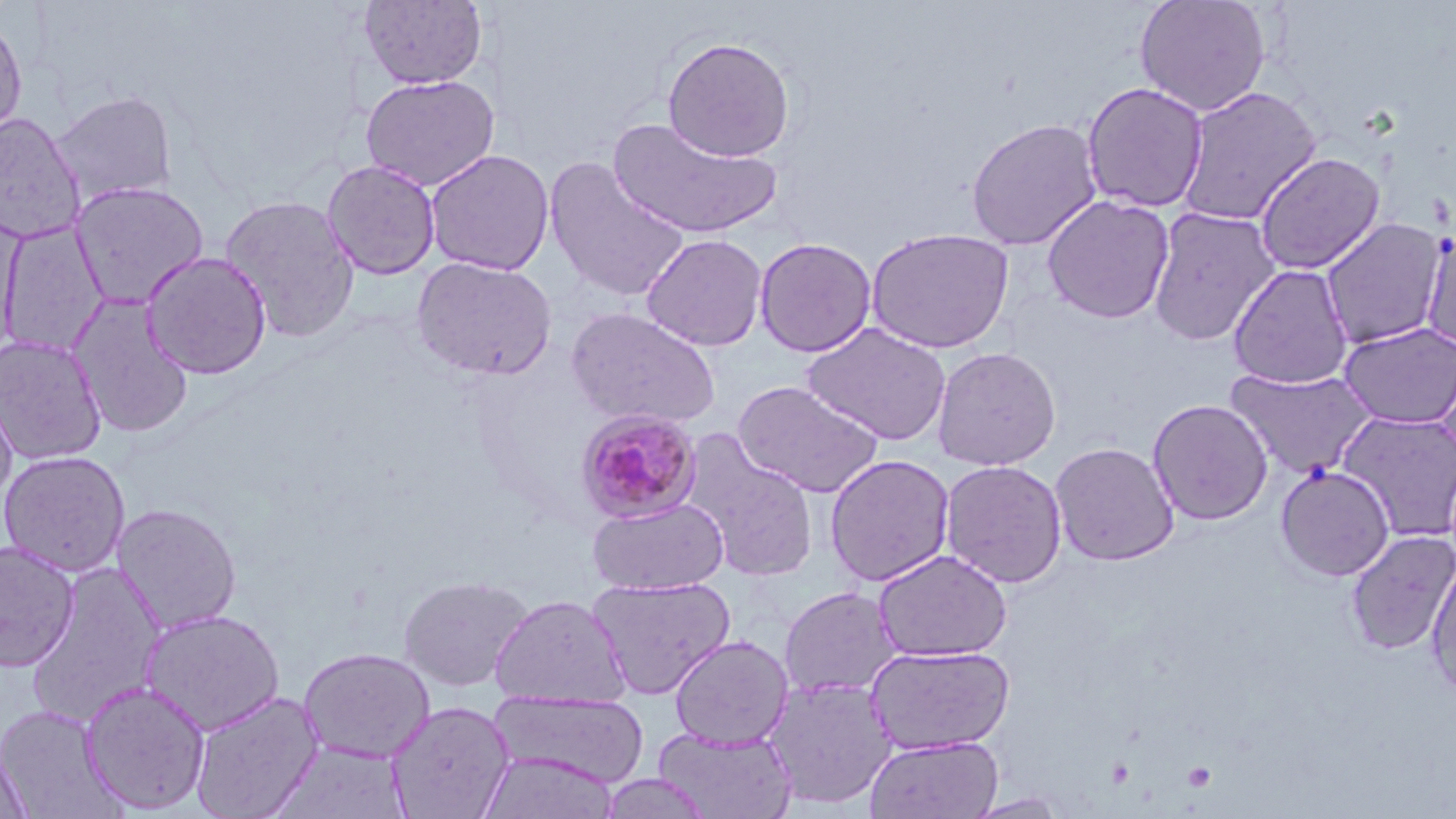
Approximate bounding boxes as (x1,y1)-(x2,y2) corner pairs in pixels. Uninfected red blood cell locations: (357,0)-(489,89), (1134,0)-(1272,117), (0,12)-(28,141), (662,37)-(796,162), (361,74)-(500,191), (1081,81)-(1209,213), (1176,85)-(1322,227), (50,90)-(178,207), (0,113)-(85,244), (607,116)-(783,240), (965,117)-(1103,250), (425,148)-(555,276), (1254,151)-(1385,275), (545,157)-(689,303), (321,160)-(441,280), (69,181)-(208,309), (219,194)-(360,344), (1041,194)-(1175,324), (1147,206)-(1281,347), (0,213)-(21,361), (1319,218)-(1449,349), (0,222)-(109,358), (1420,226)-(1456,355), (865,227)-(1014,354), (641,233)-(768,351), (754,237)-(877,357), (140,251)-(272,380), (411,256)-(557,381), (1228,263)-(1354,390), (67,294)-(195,440), (565,307)-(721,430), (802,322)-(952,446), (1338,322)-(1456,430), (0,334)-(108,465), (931,346)-(1061,471), (1432,354)-(1456,478), (1226,366)-(1378,480), (732,380)-(884,498), (0,390)-(17,507), (1147,399)-(1273,526), (1335,410)-(1456,541), (685,441)-(820,582), (1048,441)-(1180,566), (0,450)-(131,577), (824,454)-(955,587), (939,459)-(1068,589), (1275,465)-(1395,582), (588,498)-(728,595), (112,503)-(243,634), (1345,530)-(1456,655), (0,541)-(80,673), (873,549)-(1012,662), (1425,554)-(1456,700), (25,562)-(169,730), (398,575)-(532,691), (586,576)-(737,698), (779,585)-(902,700), (489,594)-(630,707), (139,608)-(285,736), (670,635)-(794,749), (866,644)-(1015,755), (298,647)-(435,763), (763,675)-(897,810), (80,680)-(211,814), (489,690)-(650,788), (190,691)-(323,819), (385,700)-(516,819), (0,704)-(123,818), (653,726)-(796,818), (864,736)-(1003,818), (0,741)-(34,819), (270,743)-(411,817), (478,751)-(619,819), (598,773)-(715,818), (962,793)-(1072,818). Plasmodium malariae-infected red blood cell locations: (575,408)-(703,525). Slide-level diagnosis: Plasmodium malariae. Optical microscopy. May-Grünwald-Giemsa-stained preparation. Image is 1456×819 pixels. One field of a larger specimen. 1000x magnification. Thin blood smear.